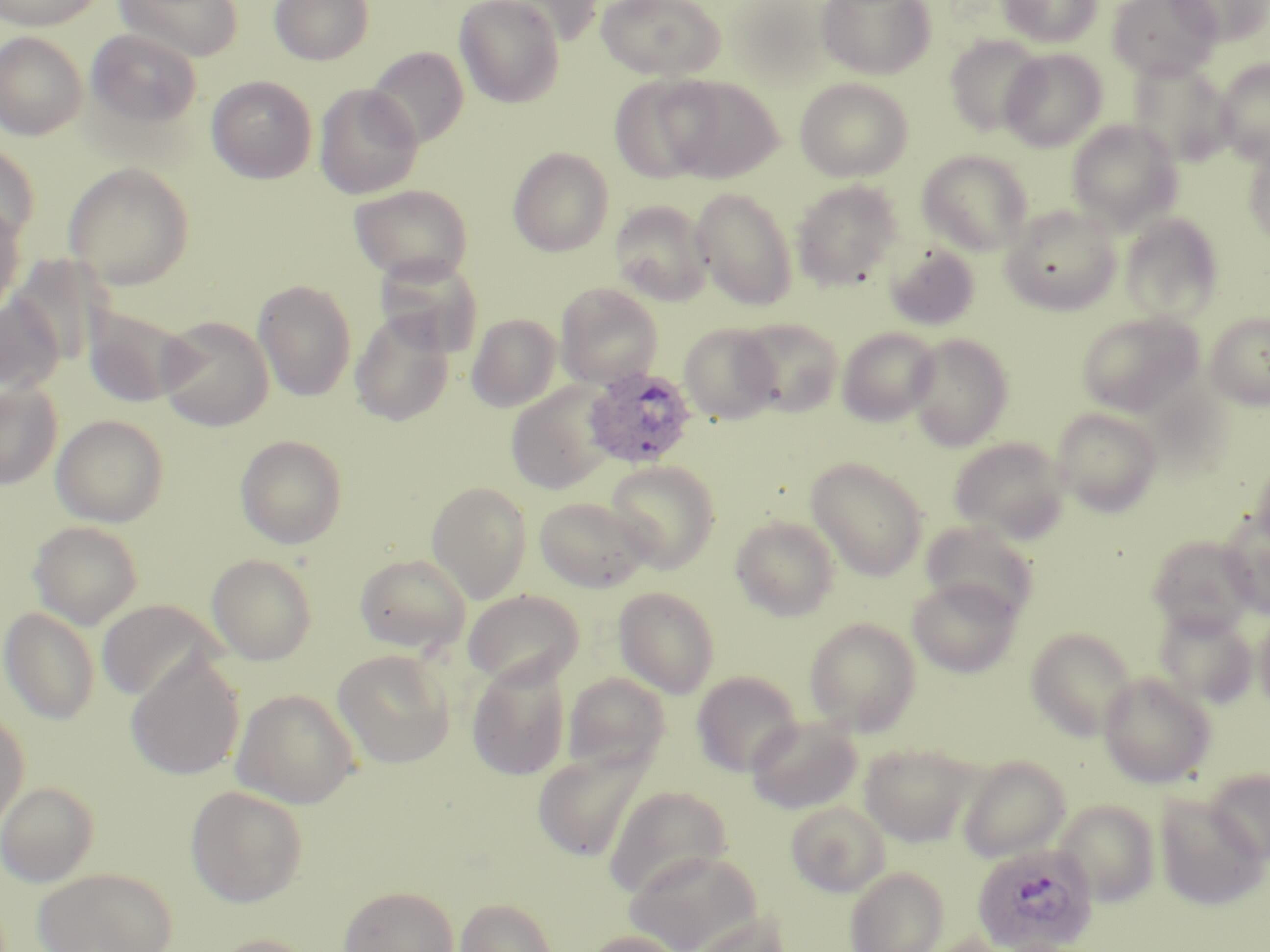

Approximate bounding boxes as [x1, y1, x2, y2] in pixels. Plasmodium ovale-infected red blood cell locations: [582, 366, 699, 469], [972, 843, 1098, 952]. Uninfected red blood cell locations: [0, 0, 106, 31], [114, 0, 243, 62], [269, 0, 374, 65], [454, 0, 565, 108], [489, 0, 606, 46], [596, 0, 726, 81], [816, 0, 936, 80], [998, 0, 1102, 48], [1108, 0, 1221, 81], [1168, 0, 1270, 46], [730, 2, 839, 89], [87, 29, 202, 128], [1, 31, 88, 141], [945, 35, 1045, 137], [367, 47, 469, 148], [1000, 48, 1107, 151], [1128, 59, 1235, 167], [1214, 59, 1270, 163], [609, 75, 716, 184], [660, 75, 783, 183], [207, 76, 317, 184], [795, 78, 913, 181], [314, 83, 423, 200], [1067, 119, 1182, 230], [0, 144, 39, 244], [1244, 146, 1270, 245], [508, 147, 614, 257], [917, 150, 1032, 255], [63, 162, 194, 290], [791, 180, 905, 290], [349, 183, 473, 283], [690, 187, 799, 311], [609, 200, 713, 305], [0, 201, 24, 317], [1001, 206, 1121, 316], [1119, 213, 1223, 324], [882, 242, 981, 331], [9, 255, 110, 367], [374, 255, 483, 357], [253, 279, 356, 401], [555, 283, 663, 388], [0, 296, 65, 394], [82, 303, 194, 407], [1205, 311, 1270, 410], [350, 312, 454, 426], [1076, 312, 1203, 417], [466, 314, 562, 412], [157, 315, 274, 431], [737, 318, 844, 417], [679, 324, 781, 424], [837, 326, 941, 427], [905, 333, 1013, 451], [0, 381, 62, 489], [505, 383, 615, 495], [1051, 408, 1163, 517], [51, 414, 170, 527], [235, 434, 348, 549], [949, 437, 1070, 543], [1253, 456, 1270, 550], [806, 457, 929, 580], [605, 460, 720, 573], [426, 481, 532, 603], [533, 497, 651, 592], [1218, 513, 1270, 617], [731, 515, 840, 621], [920, 520, 1039, 623], [28, 521, 144, 629], [1147, 535, 1256, 637], [206, 554, 317, 664], [355, 554, 471, 655], [907, 576, 1022, 678], [613, 586, 720, 699], [463, 590, 584, 689], [96, 599, 222, 702], [0, 606, 100, 725], [1154, 607, 1258, 708], [1255, 608, 1270, 715], [804, 617, 922, 736], [1026, 628, 1136, 741], [332, 649, 455, 768], [126, 653, 245, 781], [467, 658, 571, 781], [692, 671, 802, 776], [562, 672, 670, 774], [1098, 672, 1216, 788], [231, 690, 360, 809], [0, 709, 29, 834], [746, 716, 862, 814], [859, 744, 977, 847], [532, 746, 653, 862], [957, 756, 1069, 862], [1206, 768, 1270, 864], [0, 781, 99, 886], [186, 786, 308, 907], [604, 786, 731, 899], [1154, 795, 1269, 911], [1055, 799, 1160, 905], [785, 800, 890, 897], [624, 847, 763, 952], [845, 866, 948, 952], [33, 867, 176, 952], [338, 885, 459, 952], [455, 897, 558, 951], [687, 912, 791, 952], [579, 931, 689, 952], [207, 934, 319, 952]. Slide-level diagnosis: Plasmodium ovale. Light microscopy. 1000x magnification. One field of a larger specimen. Image is 1270×952 pixels. Thin blood smear. May-Grünwald-Giemsa stain.